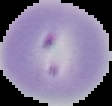
image_size: 112×106 pixels
image_type: cell region segmented out of the field of view; surrounding area masked to black
preparation: thin blood film
malaria_status: parasitized